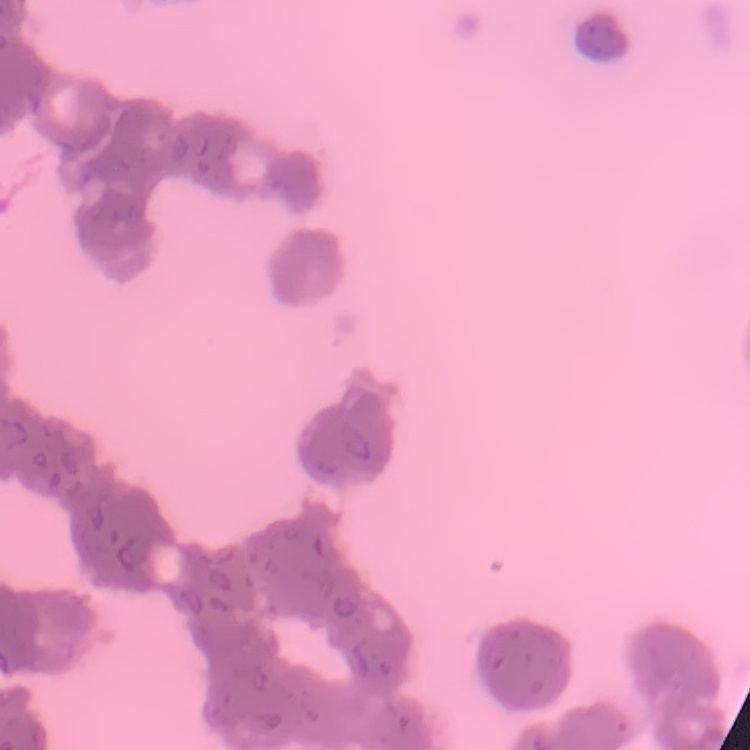

Summary:
  - Red blood cell morphology: rouleaux formation
  - Stain: Field's or Giemsa
  - Preparation: thin peripheral smear
  - Image type: one tile cut from a larger photomicrograph